Name the cell type shown.
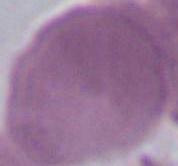

This is an erythrocyte.

Captured at 1000x magnification. Micrograph.